Locate every parasitized red blood cell.
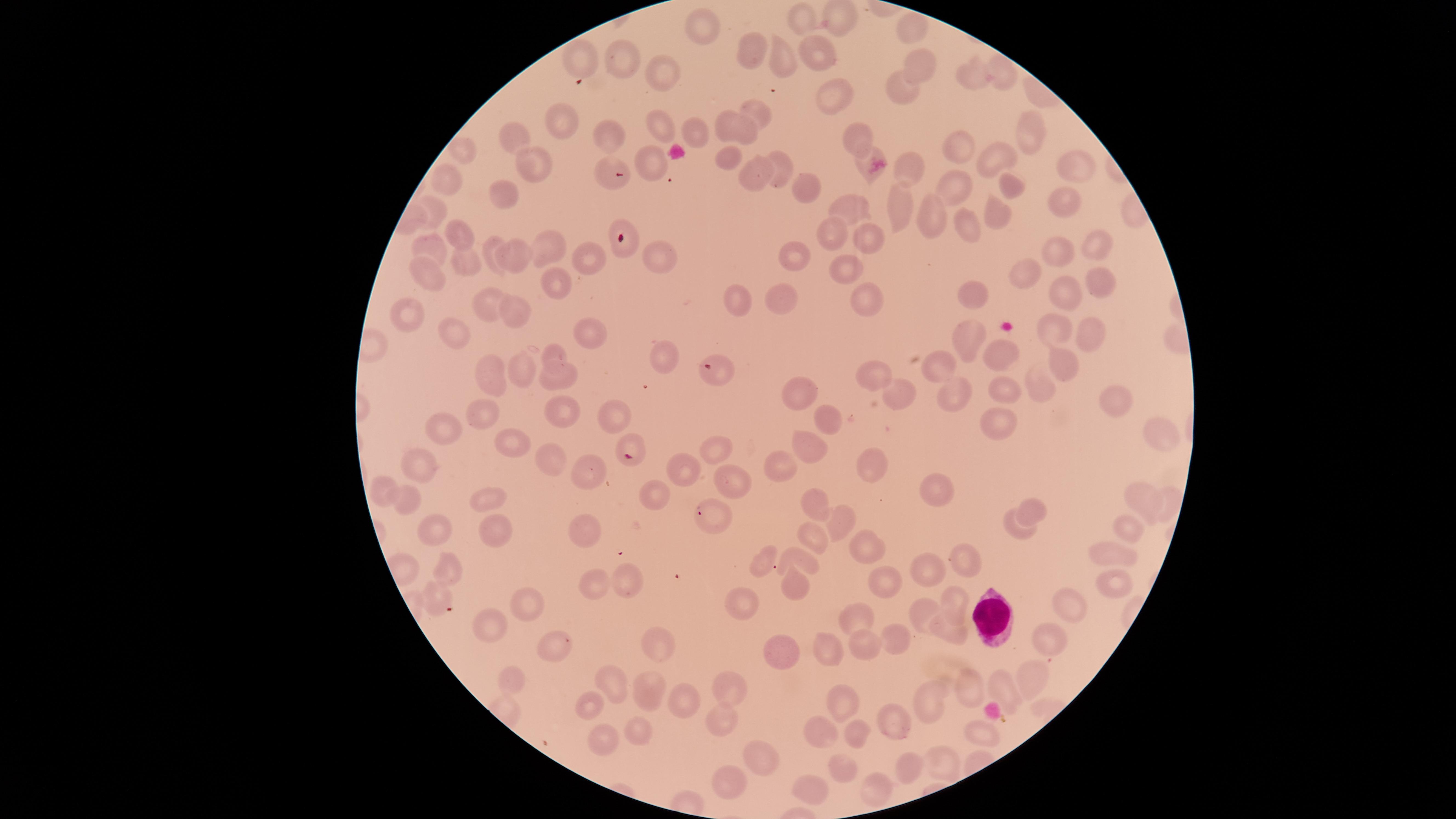

No parasitized red blood cells identified.

Approximate marker points as {x, y} in pixels.
Summary:
  - Uninfected red blood cells: {833, 20}, {803, 21}, {912, 27}, {701, 29}, {751, 49}, {817, 55}, {621, 62}, {780, 62}, {583, 63}, {922, 67}, {1001, 73}, {663, 79}, {973, 79}, {900, 89}, {832, 96}, {756, 110}, {560, 122}, {737, 128}, {656, 131}, {696, 132}, {608, 134}, {1028, 134}, {515, 138}, {859, 138}, {959, 151}, {463, 153}, {995, 157}, {728, 158}, {863, 159}, {648, 165}, {781, 165}, {1073, 165}, {534, 166}, {910, 173}, {756, 177}, {607, 179}, {448, 183}, {1013, 184}, {957, 186}, {805, 190}, {508, 195}, {1062, 202}, {849, 203}, {898, 203}, {434, 210}, {997, 211}, {928, 215}, {972, 224}, {456, 235}, {826, 236}, {867, 238}, {622, 246}, {1094, 246}, {432, 247}, {491, 247}, {547, 249}, {652, 251}, {1063, 252}, {512, 254}, {794, 254}, {584, 257}, {459, 264}, {850, 268}, {426, 272}, {1029, 273}, {1101, 283}, {556, 286}, {864, 295}, {978, 296}, {1065, 296}, {781, 302}, {735, 303}, {492, 305}, {403, 313}, {515, 314}, {1056, 324}, {459, 327}, {1083, 332}, {594, 333}, {972, 341}, {552, 355}, {655, 356}, {1002, 357}, {1062, 362}, {945, 366}, {718, 369}, {525, 370}, {870, 375}, {491, 377}, {559, 377}, {1039, 384}, {1007, 386}, {958, 389}, {803, 390}, {894, 391}, {1116, 402}, {561, 408}, {827, 411}, {483, 413}, {610, 416}, {1003, 420}, {439, 427}, {1159, 430}, {632, 440}, {510, 442}, {811, 442}, {715, 449}, {556, 460}, {868, 462}, {785, 465}, {684, 472}, {420, 474}, {580, 479}, {731, 482}, {941, 486}, {661, 494}, {383, 496}, {1146, 496}, {489, 498}, {406, 499}, {816, 501}, {1169, 501}, {1039, 508}, {715, 513}, {843, 519}, {581, 524}, {432, 528}, {1129, 528}, {496, 531}, {1013, 532}, {810, 535}, {868, 551}, {1116, 553}, {765, 558}, {801, 560}, {963, 562}, {452, 563}, {929, 571}, {592, 580}, {626, 582}, {889, 584}, {1111, 584}, {794, 586}, {439, 597}, {532, 602}, {750, 604}, {1067, 604}, {956, 605}, {924, 612}, {861, 613}, {950, 630}, {497, 631}, {561, 635}, {892, 636}, {1050, 640}, {868, 643}, {661, 647}, {828, 647}, {785, 653}, {507, 675}, {1030, 676}, {731, 687}, {1001, 687}, {616, 689}, {971, 691}, {649, 693}, {680, 696}, {842, 708}, {931, 708}, {591, 709}, {895, 719}, {721, 723}, {985, 730}, {636, 731}, {828, 734}, {854, 735}, {609, 739}, {761, 760}, {840, 762}, {943, 762}, {901, 769}, {875, 783}, {731, 787}, {812, 788}
  - White blood cells: {989, 617}
  - Capture: smartphone photograph through the microscope eyepiece
  - Field of view: single
  - Stain: Giemsa
  - Preparation: thin blood smear
  - Visible region: circular
  - Image size: 1456×819 pixels